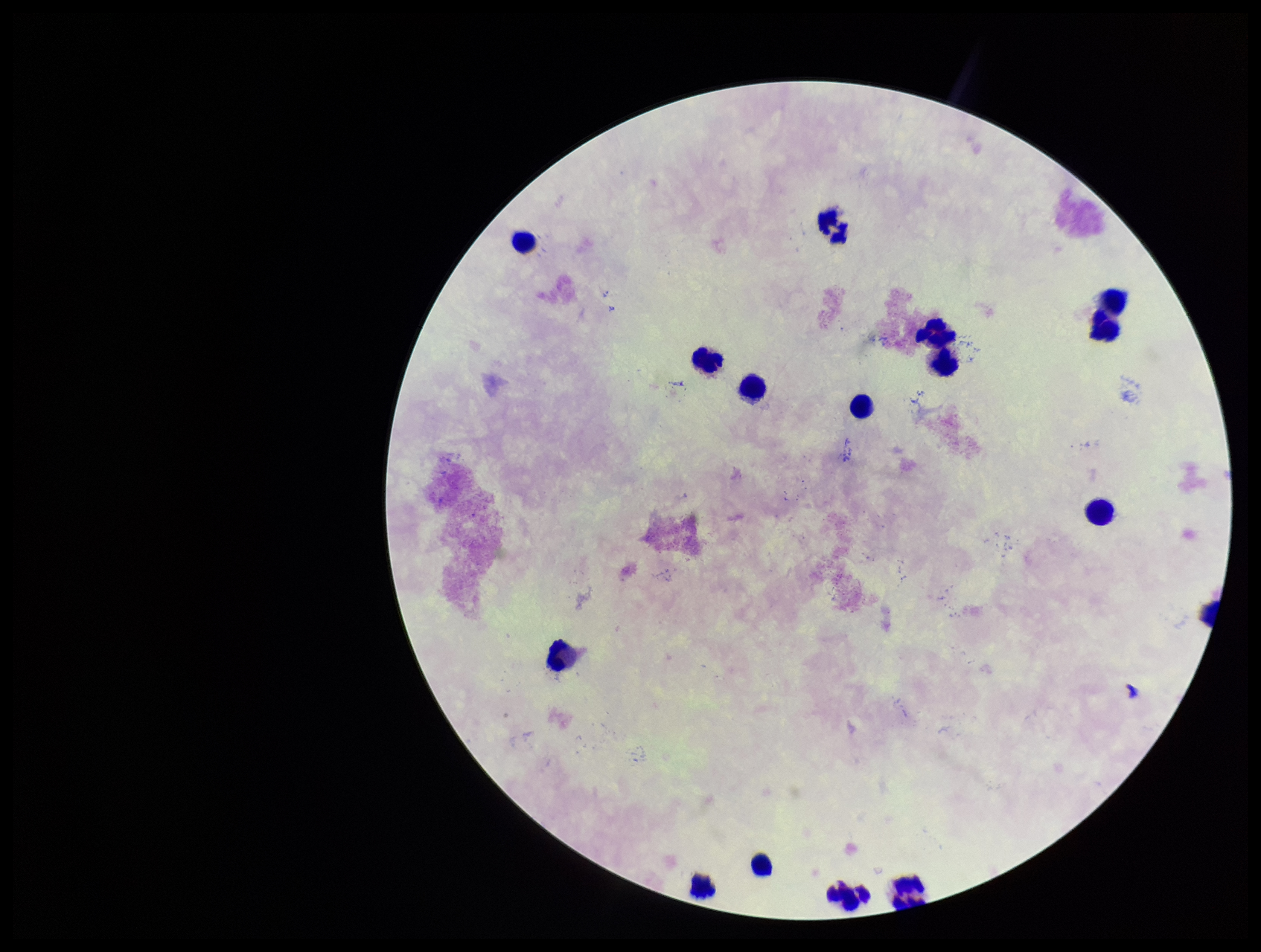

{
  "preparation": "thick blood smear",
  "patient_malaria_status": "negative",
  "capture": "smartphone photograph through the microscope eyepiece",
  "field_of_view": "one from this slide",
  "stain": "Giemsa",
  "image_size": "1261×952 pixels",
  "leukocyte_count": 16,
  "parasite_count": 0,
  "plasmodium_parasites": "none identified"
}